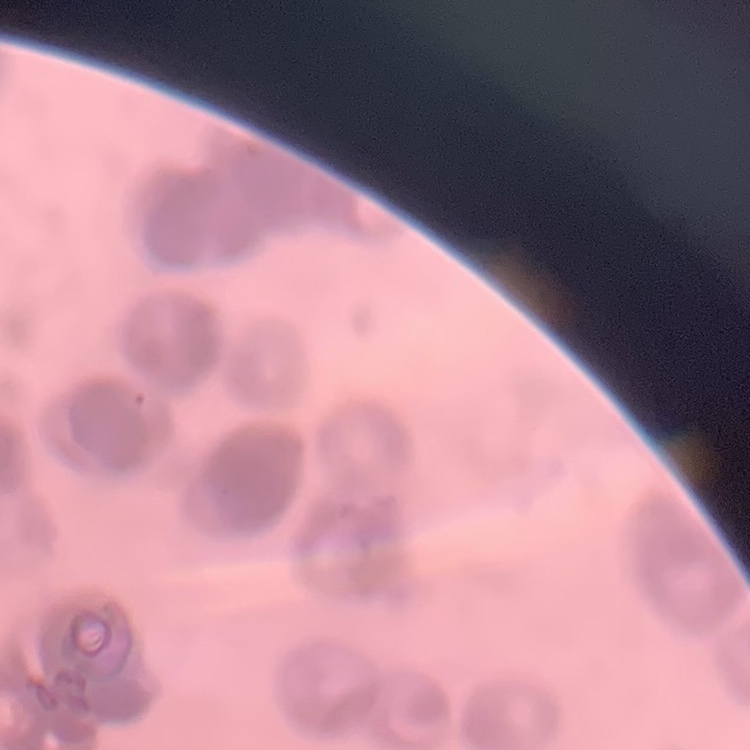

Summary:
  - Erythrocyte morphology: rouleaux formation
  - Preparation: thin peripheral smear
  - Image type: one tile cut from a larger photomicrograph
  - Stain: Field's or Giemsa